Name the parasite shown.
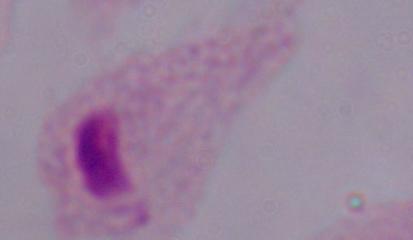

A trichomonad.

1000x magnification. Photomicrograph.